Comment on the morphology of the red blood cells.
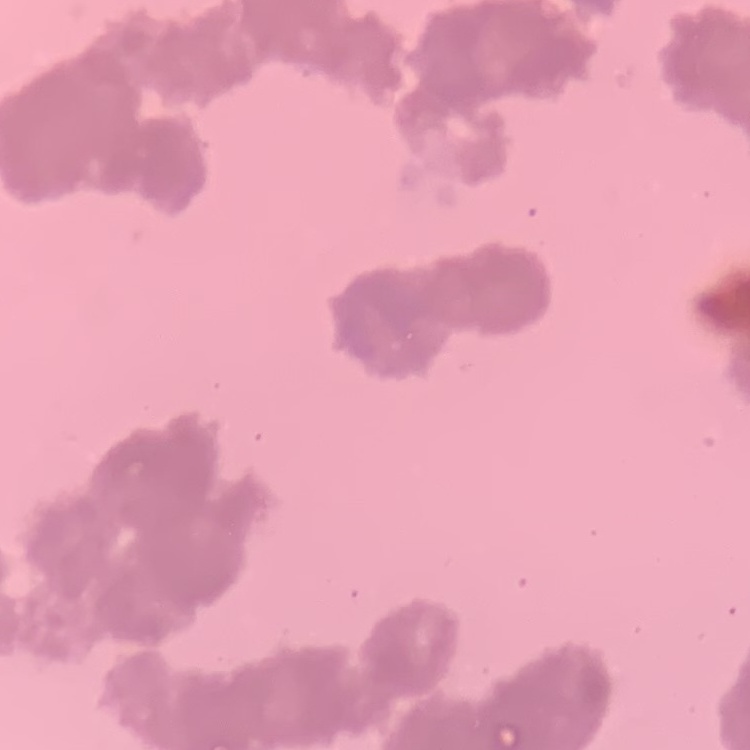
Rouleaux formation.

Thin peripheral smear. Field's or Giemsa stain. Square crop of a larger photomicrograph.